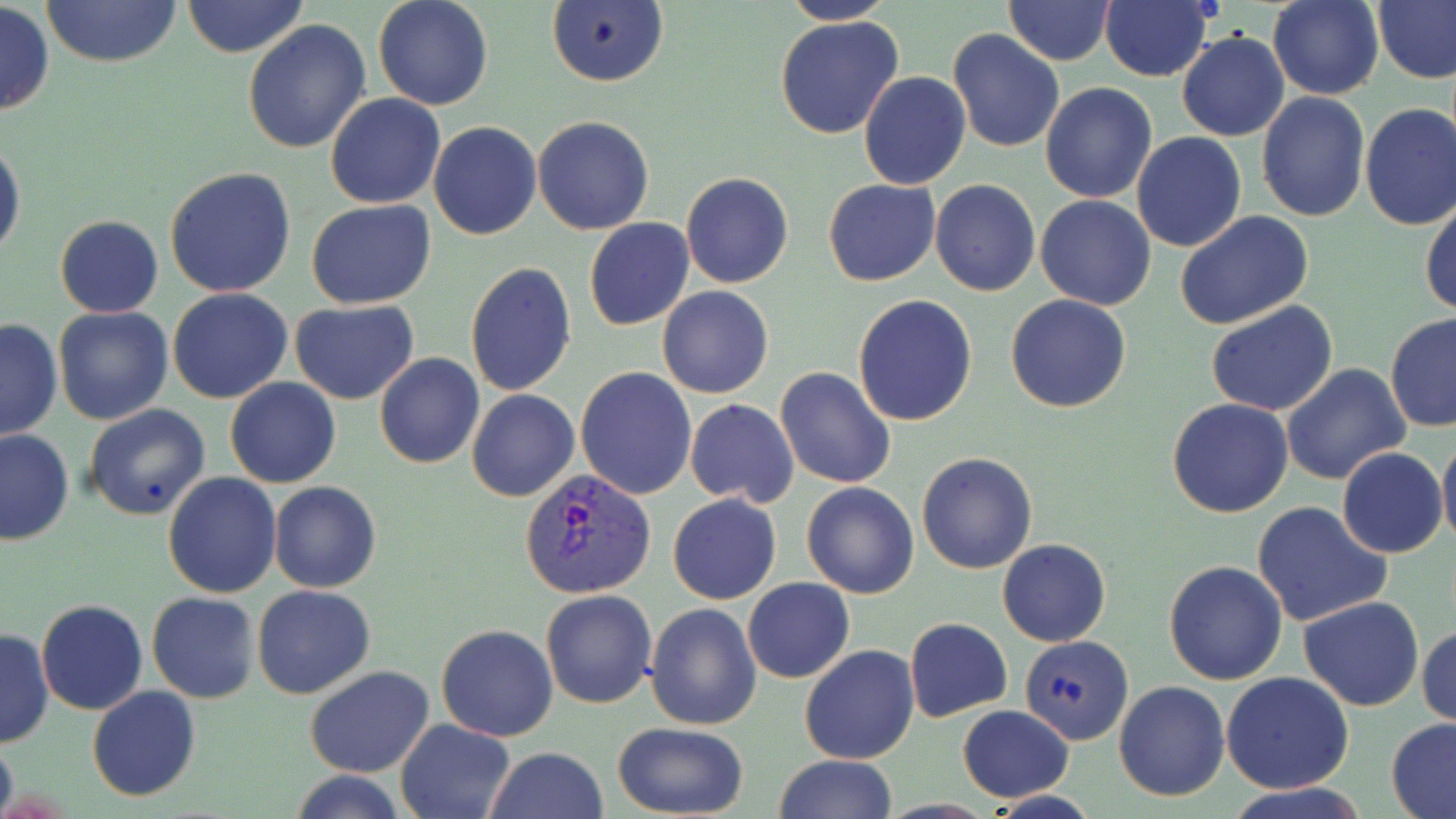

Summary:
  - Coordinate format: approximate bounding boxes as (x1, y1, x2, y2) in pixels
  - Uninfected red blood cell locations: (41, 0, 182, 67), (180, 0, 310, 58), (372, 0, 494, 111), (1004, 0, 1116, 65), (1100, 0, 1215, 83), (1267, 0, 1383, 100), (1374, 0, 1456, 85), (0, 1, 54, 117), (546, 1, 668, 88), (780, 1, 898, 24), (774, 15, 905, 140), (242, 20, 371, 155), (947, 28, 1066, 153), (1176, 32, 1290, 142), (859, 71, 970, 190), (1040, 83, 1157, 202), (1256, 92, 1371, 223), (325, 94, 445, 210), (1359, 101, 1456, 231), (532, 116, 654, 235), (429, 120, 541, 241), (1131, 132, 1246, 252), (0, 137, 24, 264), (164, 167, 297, 299), (681, 173, 794, 290), (824, 179, 940, 287), (931, 180, 1041, 296), (1035, 195, 1158, 310), (1420, 195, 1455, 317), (307, 199, 436, 309), (1174, 210, 1316, 330), (55, 215, 163, 318), (584, 218, 695, 331), (465, 261, 576, 397), (657, 285, 774, 399), (166, 287, 293, 404), (1005, 294, 1131, 413), (853, 295, 978, 427), (289, 299, 420, 403), (1205, 300, 1338, 417), (52, 305, 174, 426), (1384, 310, 1456, 432), (1, 318, 61, 442), (374, 354, 485, 470), (1280, 363, 1410, 485), (576, 367, 698, 501), (775, 367, 896, 489), (226, 378, 342, 488), (465, 389, 578, 503), (1166, 398, 1294, 518), (684, 399, 798, 507), (83, 403, 210, 520), (0, 428, 76, 544), (1437, 432, 1456, 553), (1338, 447, 1447, 559), (917, 452, 1037, 575), (163, 472, 283, 598), (268, 481, 381, 592), (801, 482, 920, 600), (666, 493, 781, 606), (1251, 501, 1392, 627), (997, 539, 1111, 647), (1163, 559, 1289, 685), (742, 577, 855, 684), (252, 585, 375, 698), (541, 590, 658, 709), (146, 591, 260, 704), (1298, 594, 1424, 711), (35, 600, 149, 716), (644, 602, 762, 731), (439, 609, 657, 724), (904, 618, 1012, 721), (436, 623, 559, 742), (1417, 624, 1456, 729), (0, 629, 52, 749), (1017, 636, 1132, 747), (799, 644, 920, 764), (304, 665, 435, 779), (1220, 672, 1353, 793), (1114, 681, 1230, 802), (87, 686, 200, 801), (956, 704, 1075, 801), (1386, 717, 1456, 819), (395, 718, 515, 819), (610, 721, 750, 817), (0, 732, 17, 819), (485, 747, 609, 819), (774, 754, 898, 819), (287, 770, 411, 819), (1228, 785, 1370, 819)
  - Plasmodium vivax-infected red blood cell locations: (520, 467, 657, 599)
  - Slide-level diagnosis: Plasmodium vivax
  - Field of view: one of a larger specimen
  - Preparation: thin blood film
  - Image size: 1456×819 pixels
  - Magnification: 1000x
  - Stain: May-Grünwald-Giemsa
  - Modality: light microscopy